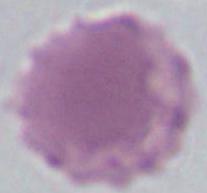
A red blood cell is seen. 1000x magnification. Micrograph.